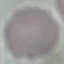
result = no malaria parasites detected
image type = automatically extracted cell patch, resized to 64 × 64 pixels
stain = Giemsa
capture = smartphone through the microscope eyepiece
preparation = thin blood smear